Assess this cell for malaria.
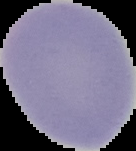

Uninfected.

Summary:
  - Image size: 136×151 pixels
  - Preparation: thin blood smear
  - Image type: cell region segmented out of the field of view; surrounding area masked to black